Name the parasite shown.
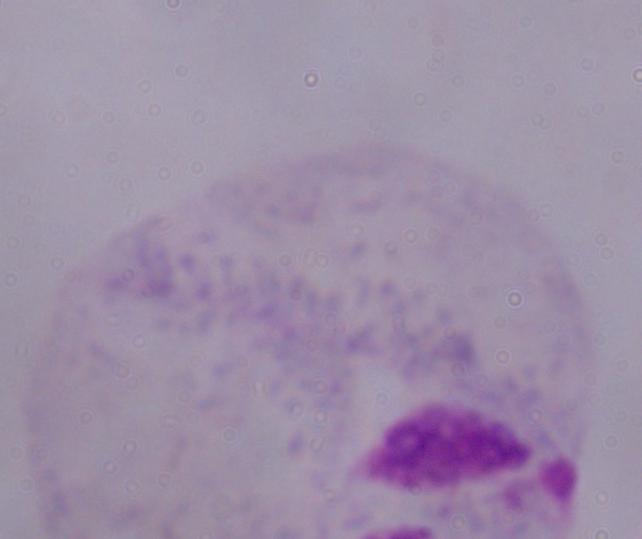
A trichomonad.

magnification: 1000x
modality: photomicrograph